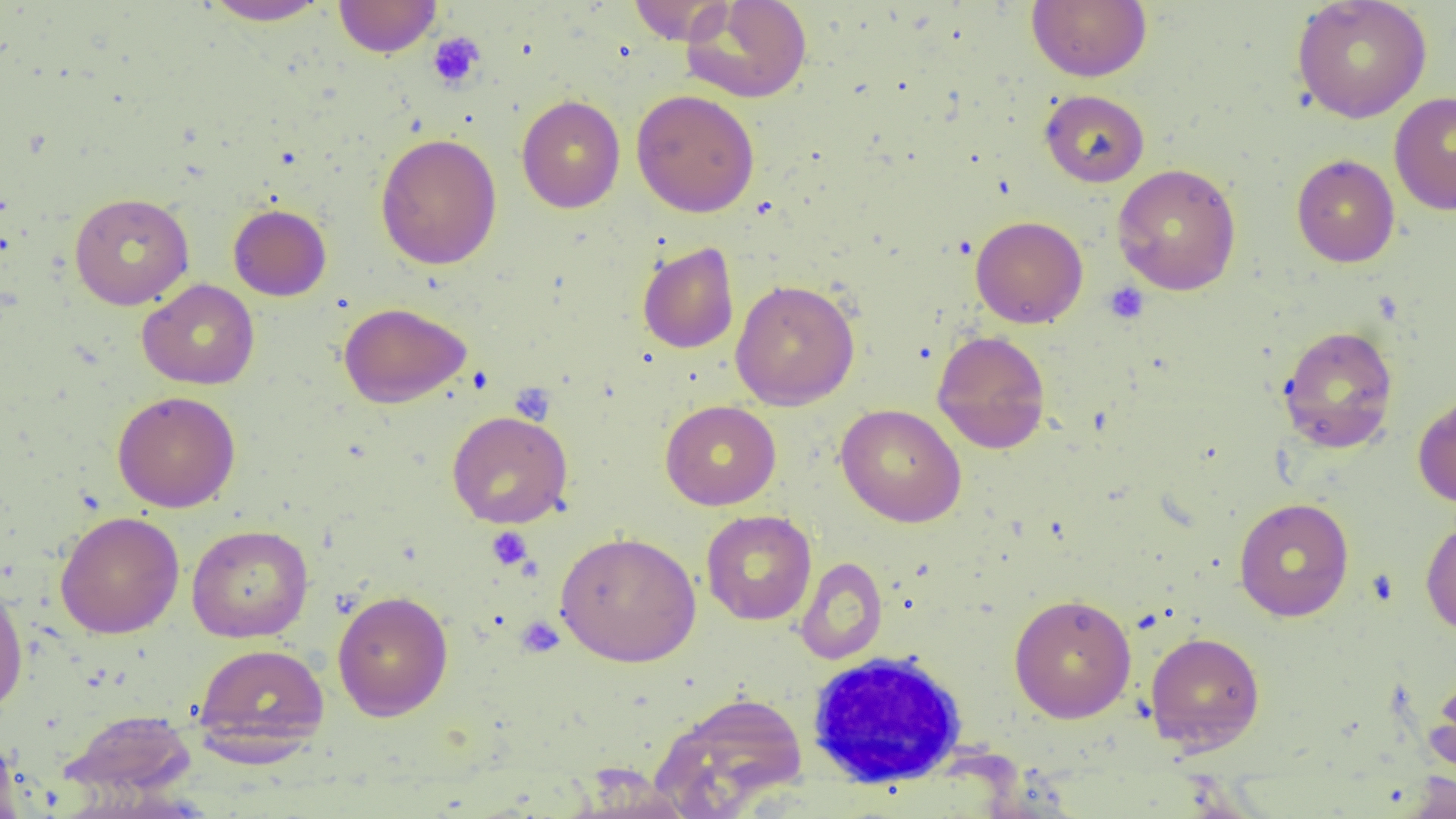

Approximate bounding boxes as (x1, y1, x2, y2) in pixels. White blood cell locations: (805, 654, 974, 794). Platelet locations: (427, 32, 485, 90), (1103, 282, 1150, 324), (511, 383, 556, 424), (486, 526, 533, 570), (515, 616, 564, 657). Uninfected red blood cell locations: (201, 0, 332, 26), (333, 0, 442, 57), (627, 0, 736, 45), (681, 0, 812, 103), (1027, 0, 1152, 82), (1291, 0, 1432, 124), (631, 89, 760, 217), (1039, 90, 1150, 187), (1389, 91, 1456, 215), (516, 94, 625, 213), (375, 133, 502, 270), (1292, 154, 1400, 267), (1112, 163, 1242, 295), (68, 192, 194, 310), (228, 204, 331, 301), (970, 215, 1088, 329), (637, 242, 739, 353), (137, 279, 260, 389), (730, 279, 860, 410), (338, 302, 471, 408), (1277, 324, 1399, 454), (931, 329, 1051, 453), (112, 391, 241, 513), (1413, 392, 1456, 508), (660, 400, 782, 510), (836, 403, 966, 527), (446, 410, 572, 528), (1233, 497, 1354, 621), (55, 510, 184, 638), (701, 510, 817, 625), (1420, 515, 1456, 637), (186, 524, 313, 643), (555, 530, 701, 667), (795, 557, 888, 664), (0, 577, 29, 715), (332, 589, 454, 721), (1009, 593, 1137, 723), (1145, 631, 1266, 754), (192, 642, 329, 755), (1425, 668, 1456, 785), (652, 692, 807, 816), (59, 710, 198, 800), (0, 739, 24, 818), (1398, 771, 1456, 819). Slide-level diagnosis: no evidence of blood parasites. Light microscopy. 1000x magnification. Thin blood film. Single field of view. Image is 1456×819 pixels.